Assess this cell for malaria.
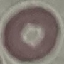
It is uninfected.

Thin blood film. Photographed with a smartphone camera at the microscope eyepiece. Automatically extracted cell patch, resized to 64 × 64 pixels. Giemsa-stained preparation.